Classify this cell by malaria status.
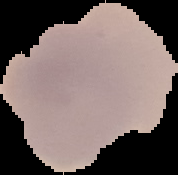
It is uninfected.

{
  "image_size": "178×175 pixels",
  "preparation": "thin blood film",
  "image_type": "segmented cell region on a black background"
}